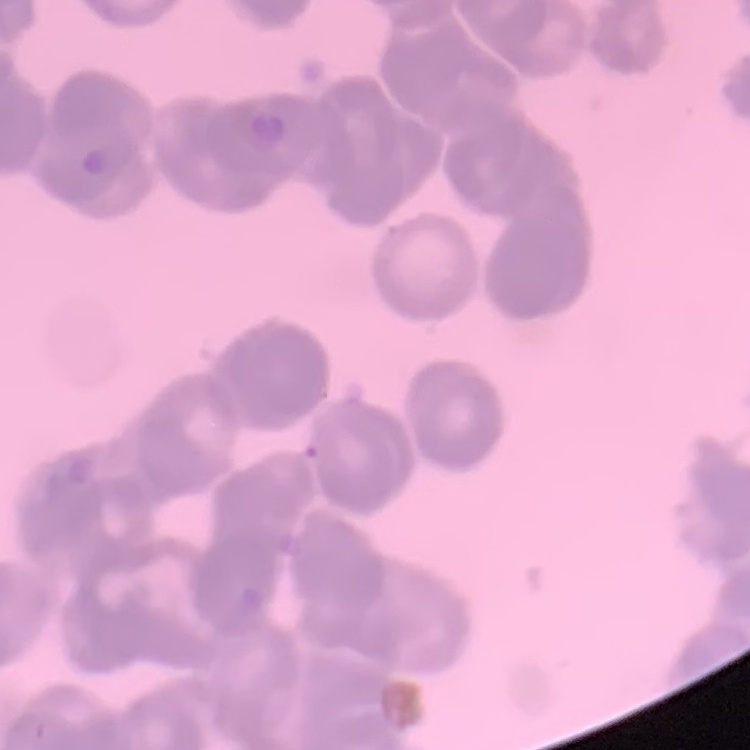
Summary:
  - Erythrocyte morphology: rouleaux formation
  - Image type: square crop of a larger photomicrograph
  - Preparation: thin blood film
  - Stain: Field's or Giemsa